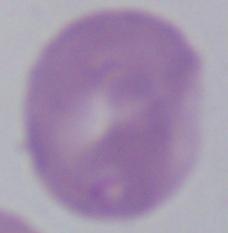

identification = Babesia
modality = photomicrograph
magnification = 1000x